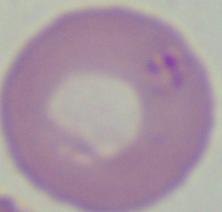
Summary:
  - Magnification: 1000x
  - Identification: Babesia
  - Modality: micrograph